Assess this cell for malaria.
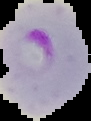
Parasitized.

Image is 91×121 pixels. Cell region segmented out of the field of view; the surrounding area is masked to black. From a thin blood smear.